Locate every blood parasite and identify its species.
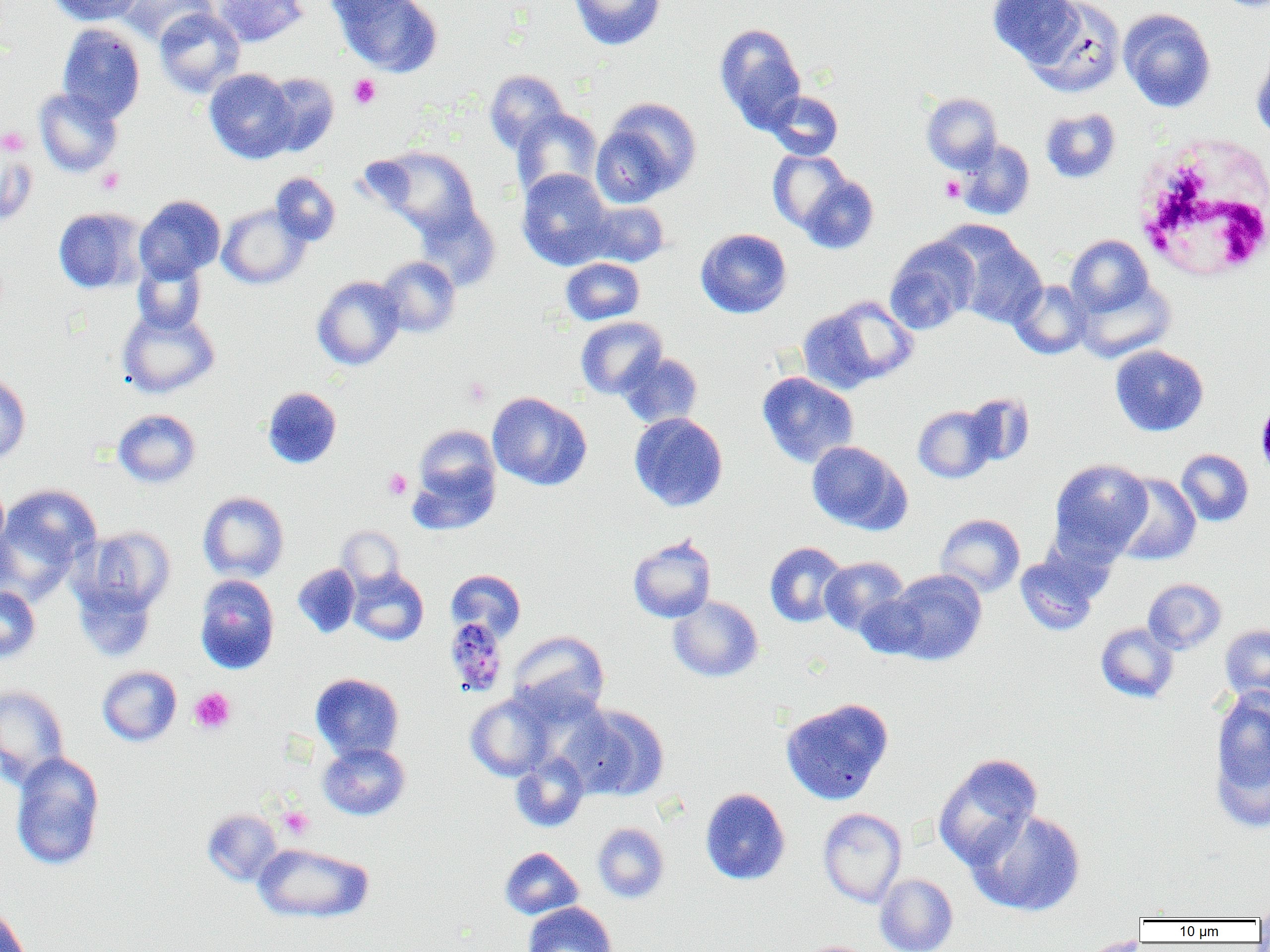

Approximate bounding boxes as (x1, y1, x2, y2) in pixels.
Plasmodium malariae-infected red blood cells: (444, 617, 508, 697).
No Plasmodium falciparum, Plasmodium ovale, Plasmodium vivax, Babesia divergens, or Trypanosoma brucei observed.

Summary:
  - Platelet locations: (349, 74, 381, 109), (0, 126, 30, 155), (97, 167, 125, 194), (941, 176, 964, 202), (463, 378, 491, 407), (384, 469, 411, 499), (190, 688, 235, 733), (278, 807, 313, 839)
  - White blood cell locations: (1131, 136, 1269, 281)
  - Uninfected red blood cell locations: (49, 0, 142, 25), (114, 0, 216, 46), (212, 0, 308, 46), (322, 0, 418, 24), (336, 0, 443, 78), (569, 0, 666, 51), (989, 0, 1083, 69), (1027, 0, 1125, 97), (1214, 0, 1270, 11), (154, 8, 245, 98), (1118, 8, 1216, 112), (57, 24, 145, 123), (715, 24, 807, 132), (1251, 50, 1270, 142), (204, 68, 297, 163), (485, 69, 568, 155), (262, 72, 339, 156), (34, 87, 123, 178), (766, 90, 843, 160), (921, 93, 1002, 172), (593, 98, 702, 205), (512, 108, 603, 201), (1041, 108, 1121, 183), (956, 139, 1035, 220), (367, 145, 480, 237), (0, 149, 37, 227), (768, 149, 851, 232), (517, 169, 615, 270), (270, 172, 340, 245), (799, 175, 879, 254), (134, 195, 225, 283), (580, 200, 670, 267), (414, 201, 501, 291), (217, 203, 311, 290), (53, 207, 146, 294), (945, 227, 1048, 328), (695, 228, 792, 318), (1066, 234, 1154, 318), (885, 236, 980, 335), (376, 256, 460, 337), (132, 257, 207, 335), (561, 258, 644, 325), (1074, 274, 1175, 363), (312, 275, 405, 371), (1009, 280, 1091, 359), (799, 295, 918, 392), (117, 307, 220, 399), (575, 317, 667, 399), (1110, 345, 1208, 436), (617, 352, 703, 428), (757, 371, 858, 467), (0, 372, 31, 465), (262, 387, 342, 469), (487, 392, 592, 490), (963, 393, 1035, 466), (913, 405, 996, 483), (113, 409, 201, 488), (629, 412, 728, 511), (413, 425, 501, 508), (806, 440, 910, 534), (1176, 449, 1254, 526), (1049, 458, 1152, 561), (407, 464, 498, 536), (1111, 473, 1202, 566), (0, 476, 9, 559), (0, 484, 101, 595), (198, 491, 289, 582), (935, 513, 1025, 597), (77, 526, 176, 617), (337, 526, 405, 590), (628, 534, 716, 623), (765, 542, 849, 627), (1015, 549, 1105, 636), (820, 557, 908, 636), (292, 564, 360, 638), (349, 569, 429, 645), (446, 569, 526, 641), (885, 569, 987, 665), (194, 574, 279, 674), (72, 577, 157, 662), (1143, 578, 1226, 654), (0, 586, 41, 663), (855, 593, 929, 660), (668, 595, 763, 682), (1095, 622, 1178, 703), (1219, 624, 1270, 705), (508, 630, 610, 720), (97, 665, 182, 747), (310, 673, 404, 761), (0, 685, 70, 788), (1209, 688, 1270, 827), (465, 692, 556, 781), (780, 697, 894, 805), (565, 705, 669, 800), (318, 741, 411, 821), (10, 752, 106, 872), (510, 752, 589, 832), (933, 753, 1042, 870), (700, 787, 791, 885), (203, 808, 283, 885), (818, 808, 907, 907), (967, 809, 1086, 917), (593, 822, 669, 903), (253, 842, 374, 924), (500, 847, 583, 920), (875, 873, 958, 952), (522, 902, 617, 952), (0, 904, 31, 952), (1079, 935, 1153, 952), (800, 941, 874, 952)
  - Slide-level diagnosis: Plasmodium malariae
  - Field of view: single
  - Magnification: 1000x
  - Preparation: thin blood smear
  - Image size: 1270×952 pixels
  - Modality: light microscopy